Mark where leukocytes are.
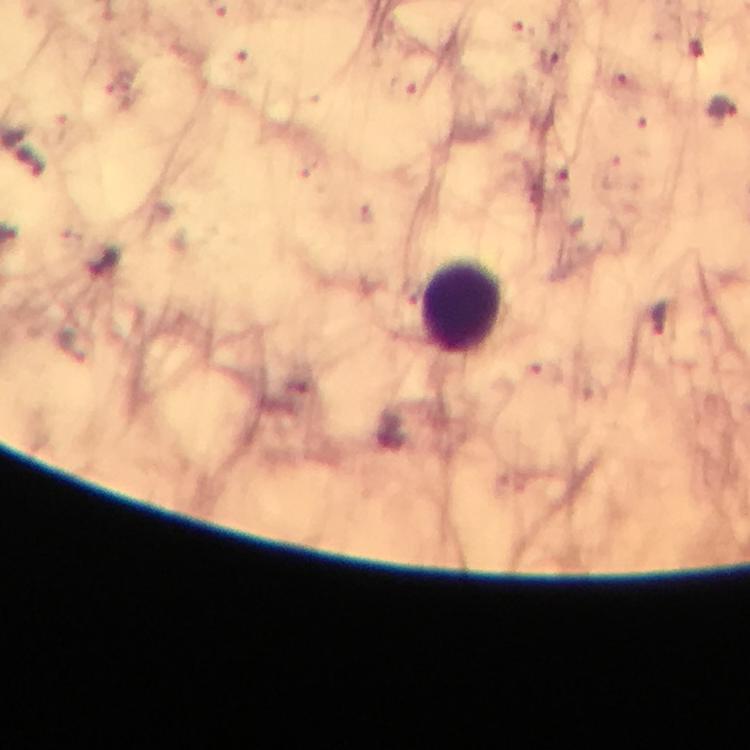

Approximate centers as {x, y} in pixels.
Leukocytes: {461, 306}.

Malaria parasite locations: {550, 61}, {245, 67}, {618, 84}, {402, 87}, {721, 108}, {554, 179}, {659, 321}. Giemsa stain. Smartphone photograph taken through a microscope. A crop from one field of view. 100x magnification. Thick blood film. Image is 750×750 pixels. From a diagnostic examination for malaria. Immersion oil was used.